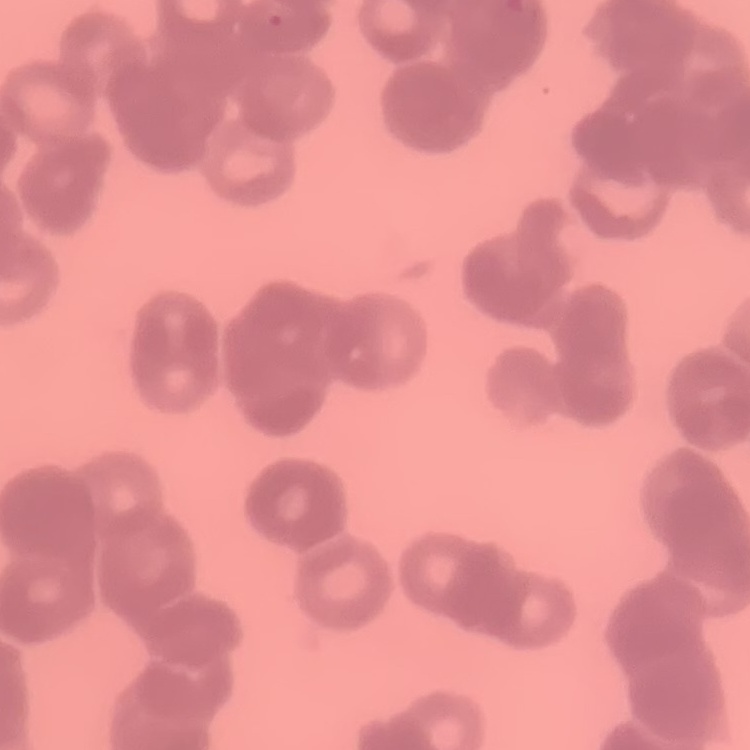

Summary:
  - Red blood cell morphology: rouleaux formation
  - Preparation: thin blood film
  - Stain: Field's or Giemsa
  - Image type: one tile cut from a larger photomicrograph